Give the extent of all Plasmodium malariae-infected red blood cells.
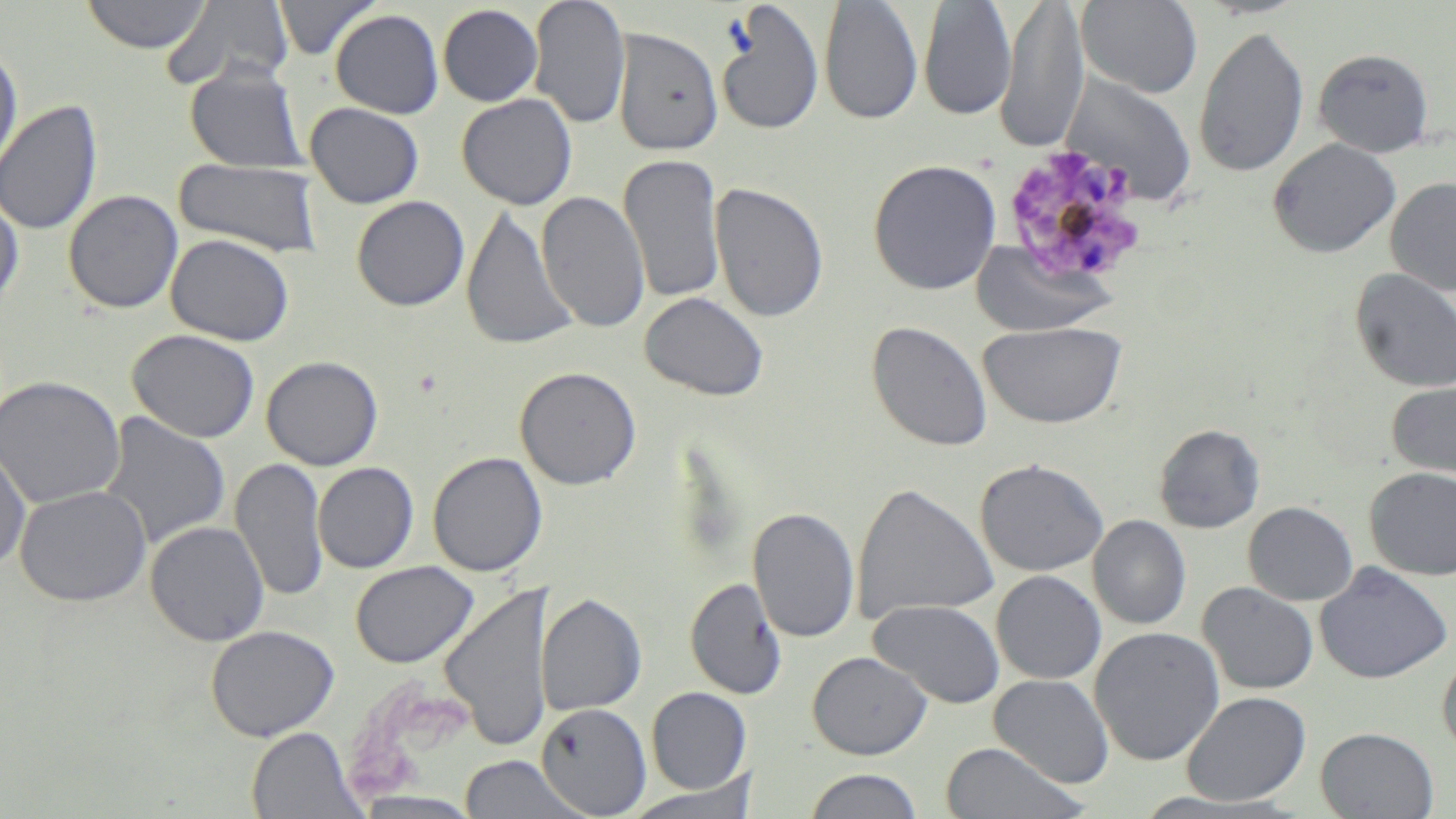
Approximate bounding boxes as named x1/y1/x2/y2 corners in pixels.
Plasmodium malariae-infected red blood cells: (x1=1000, y1=147, x2=1146, y2=287).

Uninfected red blood cell locations: (x1=80, y1=0, x2=213, y2=53), (x1=273, y1=0, x2=381, y2=60), (x1=528, y1=0, x2=631, y2=129), (x1=996, y1=0, x2=1089, y2=152), (x1=1076, y1=0, x2=1204, y2=98), (x1=163, y1=1, x2=292, y2=91), (x1=819, y1=1, x2=924, y2=125), (x1=919, y1=1, x2=1018, y2=120), (x1=716, y1=2, x2=825, y2=136), (x1=438, y1=4, x2=543, y2=106), (x1=330, y1=9, x2=444, y2=118), (x1=1193, y1=25, x2=1309, y2=179), (x1=612, y1=27, x2=724, y2=156), (x1=0, y1=47, x2=23, y2=176), (x1=1313, y1=48, x2=1435, y2=157), (x1=185, y1=62, x2=307, y2=173), (x1=1060, y1=72, x2=1198, y2=206), (x1=456, y1=93, x2=578, y2=210), (x1=0, y1=99, x2=104, y2=235), (x1=305, y1=102, x2=424, y2=208), (x1=1268, y1=138, x2=1401, y2=258), (x1=619, y1=152, x2=726, y2=305), (x1=174, y1=158, x2=324, y2=258), (x1=868, y1=159, x2=1002, y2=295), (x1=1385, y1=177, x2=1456, y2=296), (x1=710, y1=181, x2=828, y2=323), (x1=63, y1=189, x2=184, y2=314), (x1=536, y1=190, x2=650, y2=333), (x1=0, y1=192, x2=23, y2=307), (x1=351, y1=196, x2=470, y2=311), (x1=461, y1=205, x2=578, y2=352), (x1=166, y1=234, x2=295, y2=346), (x1=970, y1=240, x2=1119, y2=337), (x1=1350, y1=268, x2=1456, y2=394), (x1=639, y1=291, x2=769, y2=402), (x1=866, y1=320, x2=994, y2=452), (x1=977, y1=321, x2=1127, y2=428), (x1=127, y1=329, x2=260, y2=443), (x1=261, y1=355, x2=383, y2=471), (x1=514, y1=366, x2=641, y2=490), (x1=0, y1=375, x2=125, y2=509), (x1=1386, y1=379, x2=1456, y2=482), (x1=99, y1=412, x2=232, y2=551), (x1=1154, y1=423, x2=1265, y2=534), (x1=0, y1=439, x2=32, y2=574), (x1=427, y1=451, x2=548, y2=578), (x1=230, y1=457, x2=329, y2=602), (x1=974, y1=458, x2=1108, y2=577), (x1=313, y1=462, x2=419, y2=573), (x1=1364, y1=467, x2=1456, y2=579), (x1=852, y1=481, x2=998, y2=623), (x1=15, y1=485, x2=151, y2=607), (x1=1243, y1=501, x2=1357, y2=606), (x1=748, y1=507, x2=860, y2=643), (x1=1088, y1=515, x2=1191, y2=630), (x1=145, y1=520, x2=269, y2=646), (x1=350, y1=560, x2=478, y2=668), (x1=1314, y1=562, x2=1453, y2=684), (x1=991, y1=570, x2=1106, y2=685), (x1=685, y1=577, x2=788, y2=700), (x1=440, y1=581, x2=552, y2=753), (x1=1197, y1=582, x2=1319, y2=695), (x1=536, y1=593, x2=647, y2=716), (x1=869, y1=599, x2=1005, y2=709), (x1=205, y1=625, x2=340, y2=742), (x1=1089, y1=626, x2=1225, y2=766), (x1=1437, y1=650, x2=1456, y2=758), (x1=807, y1=651, x2=931, y2=760), (x1=988, y1=674, x2=1114, y2=788), (x1=646, y1=687, x2=751, y2=794), (x1=1181, y1=691, x2=1311, y2=806), (x1=536, y1=702, x2=651, y2=816), (x1=247, y1=726, x2=365, y2=818), (x1=1316, y1=727, x2=1439, y2=818), (x1=939, y1=741, x2=1088, y2=819), (x1=457, y1=754, x2=588, y2=818), (x1=803, y1=769, x2=924, y2=819), (x1=618, y1=781, x2=761, y2=818). Slide-level diagnosis: Plasmodium malariae. Captured at 1000x magnification. May-Grünwald-Giemsa stain. Thin blood smear. Light microscopy. Image is 1456×819 pixels. One field of a larger specimen.